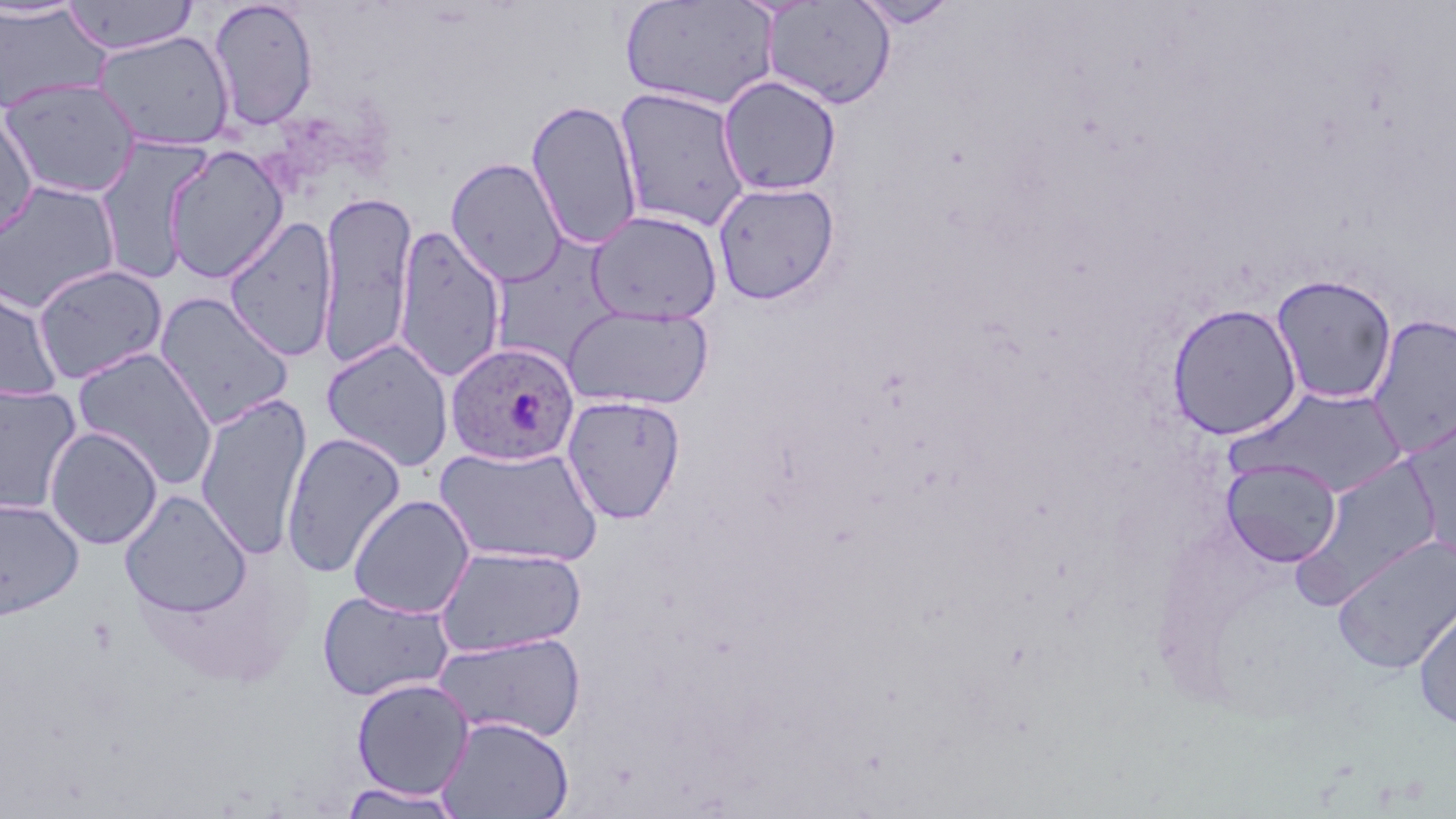
Approximate bounding boxes as named x1/y1/x2/y2 corners in pixels. Uninfected red blood cell locations: (x1=0, y1=0, x2=89, y2=22), (x1=62, y1=0, x2=199, y2=55), (x1=208, y1=0, x2=319, y2=130), (x1=619, y1=1, x2=777, y2=112), (x1=761, y1=1, x2=897, y2=110), (x1=852, y1=1, x2=960, y2=29), (x1=0, y1=4, x2=111, y2=115), (x1=92, y1=30, x2=236, y2=151), (x1=717, y1=75, x2=842, y2=196), (x1=1, y1=78, x2=141, y2=198), (x1=614, y1=86, x2=751, y2=232), (x1=526, y1=99, x2=643, y2=251), (x1=0, y1=111, x2=39, y2=243), (x1=94, y1=137, x2=212, y2=285), (x1=163, y1=144, x2=289, y2=283), (x1=445, y1=157, x2=567, y2=287), (x1=0, y1=179, x2=121, y2=315), (x1=712, y1=181, x2=840, y2=305), (x1=317, y1=191, x2=417, y2=370), (x1=587, y1=210, x2=723, y2=324), (x1=223, y1=216, x2=338, y2=361), (x1=393, y1=225, x2=507, y2=382), (x1=499, y1=240, x2=619, y2=367), (x1=31, y1=263, x2=169, y2=385), (x1=1270, y1=273, x2=1398, y2=405), (x1=0, y1=283, x2=64, y2=402), (x1=153, y1=291, x2=295, y2=429), (x1=1166, y1=302, x2=1302, y2=440), (x1=562, y1=304, x2=715, y2=410), (x1=1367, y1=313, x2=1456, y2=458), (x1=321, y1=338, x2=455, y2=472), (x1=71, y1=346, x2=220, y2=490), (x1=1, y1=382, x2=83, y2=516), (x1=1232, y1=385, x2=1410, y2=499), (x1=194, y1=391, x2=313, y2=559), (x1=561, y1=394, x2=686, y2=524), (x1=44, y1=426, x2=163, y2=550), (x1=281, y1=431, x2=407, y2=578), (x1=435, y1=443, x2=604, y2=567), (x1=1221, y1=458, x2=1341, y2=566), (x1=1294, y1=458, x2=1444, y2=606), (x1=119, y1=490, x2=252, y2=618), (x1=348, y1=494, x2=475, y2=618), (x1=0, y1=498, x2=84, y2=621), (x1=1333, y1=534, x2=1456, y2=672), (x1=434, y1=545, x2=588, y2=658), (x1=317, y1=589, x2=455, y2=702), (x1=1413, y1=592, x2=1456, y2=732), (x1=434, y1=631, x2=587, y2=743), (x1=350, y1=677, x2=475, y2=801), (x1=436, y1=715, x2=574, y2=819), (x1=338, y1=782, x2=466, y2=818). Plasmodium ovale-infected red blood cell locations: (x1=446, y1=342, x2=580, y2=466). Slide-level diagnosis: Plasmodium ovale. Single field of view. Optical microscopy. Image is 1456×819 pixels. 1000x magnification. May-Grünwald-Giemsa-stained preparation. Thin blood smear.